Report the malaria status of this cell.
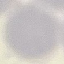
Uninfected.

Giemsa-stained preparation. Thin blood film. Acquired by smartphone through the microscope eyepiece. Cell patch, automatically extracted from a larger field of view and resized to 64 × 64 pixels.